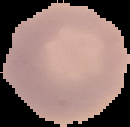

{
  "result": "no Plasmodium parasites seen",
  "preparation": "thin blood film",
  "image_type": "segmented cell region on a black background",
  "image_size": "130×127 pixels"
}